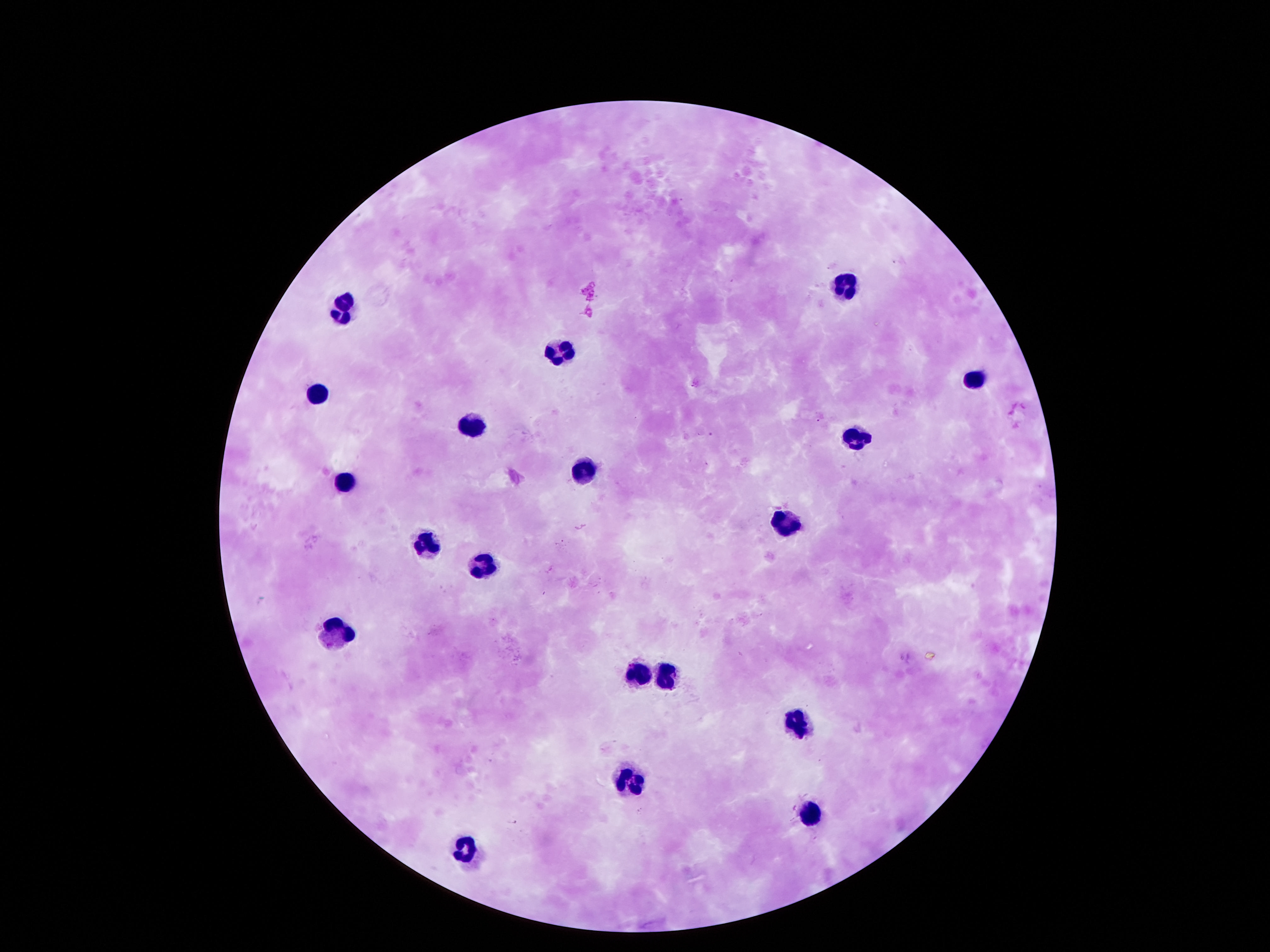

{
  "field_of_view": "one from this slide",
  "patient_malaria_status": "uninfected",
  "capture": "smartphone camera through the microscope eyepiece",
  "preparation": "thick peripheral-blood smear",
  "leukocyte_locations": "approximate centers as (x, y) in pixels: (848, 283), (340, 315), (558, 351), (975, 377), (318, 393), (468, 423), (854, 435), (583, 468), (343, 479), (785, 516), (427, 542), (477, 567), (334, 632), (639, 670), (664, 673), (798, 723), (633, 779), (810, 815), (462, 850)",
  "magnification": "100x",
  "stain": "Giemsa",
  "image_size": "1270×952 pixels"
}